Assess for Plasmodium parasites.
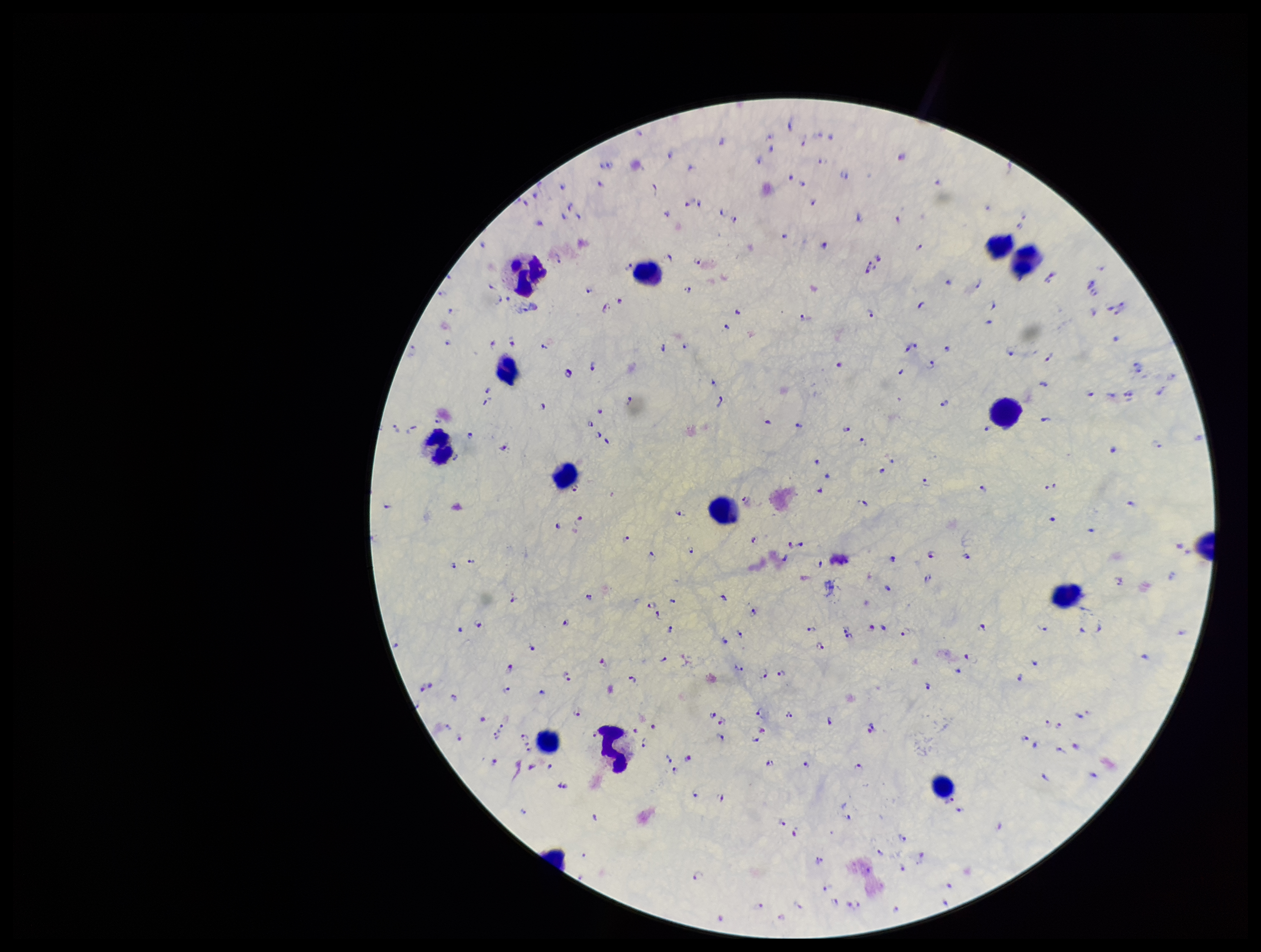

Seen.

Summary:
  - Field of view: single
  - Species reported for this patient: Plasmodium falciparum
  - Patient malaria status: positive
  - Stain: Giemsa
  - Capture: smartphone photograph through the microscope eyepiece
  - Image size: 1261×952 pixels
  - Parasite count: 219
  - Leukocyte count: 14
  - Preparation: thick smear